Report the malaria status of this cell.
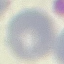
Uninfected.

Summary:
  - Capture: smartphone through the microscope eyepiece
  - Preparation: thin blood smear
  - Stain: Giemsa
  - Image type: cell patch, automatically extracted from a larger field of view and resized to 64 × 64 pixels